Assess for malaria.
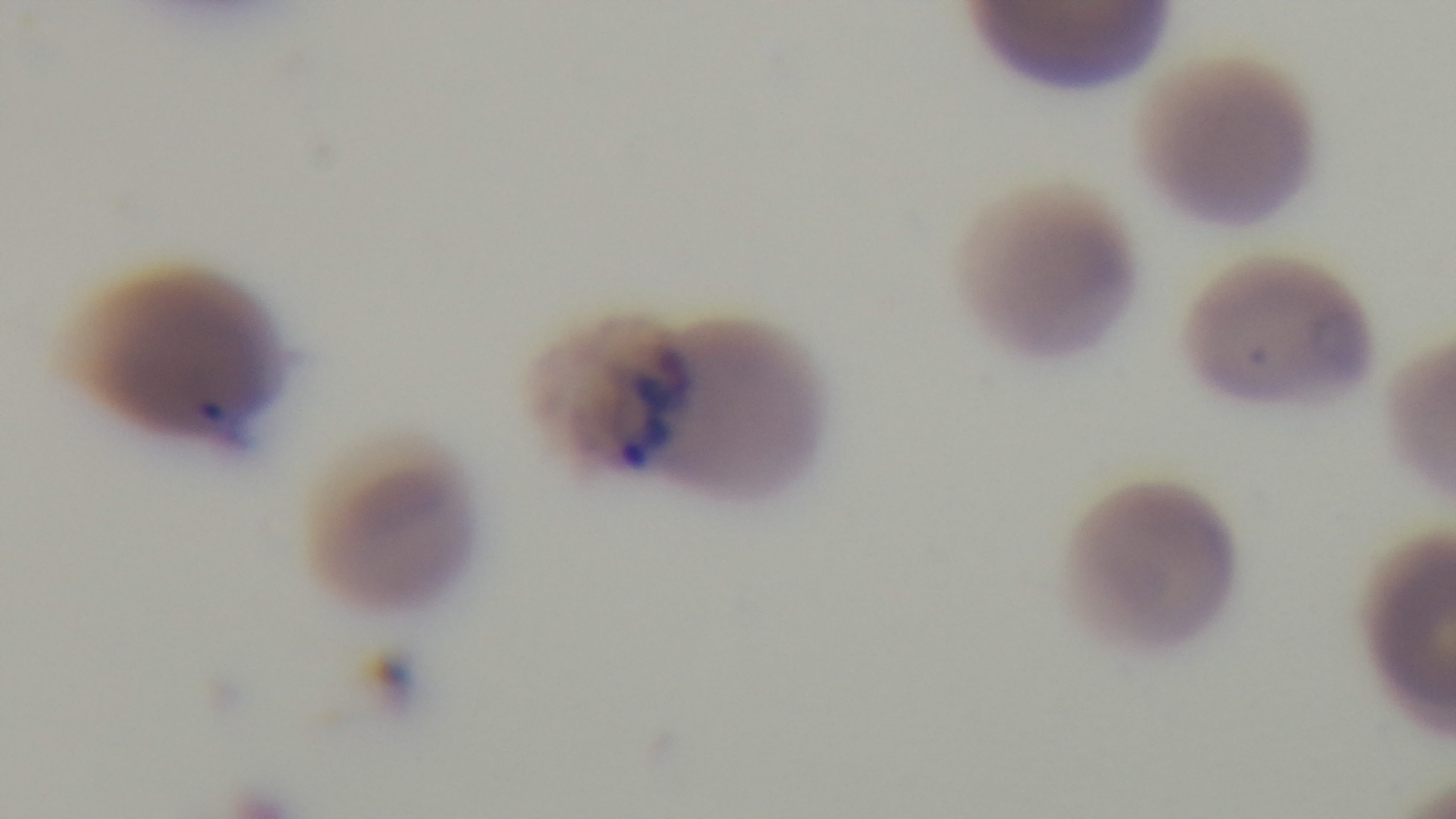
Infected.

Summary:
  - Field of view: single
  - Preparation: thin blood film
  - Capture: mounted 4K digital camera
  - Objective: 100x oil immersion
  - Modality: light microscopy
  - Stain: Giemsa